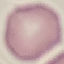
result = no malaria parasites detected
preparation = thin blood film
stain = Giemsa
image type = automatically extracted cell patch, resized to 64 × 64 pixels
capture = smartphone through the microscope eyepiece